Point out each malaria parasite.
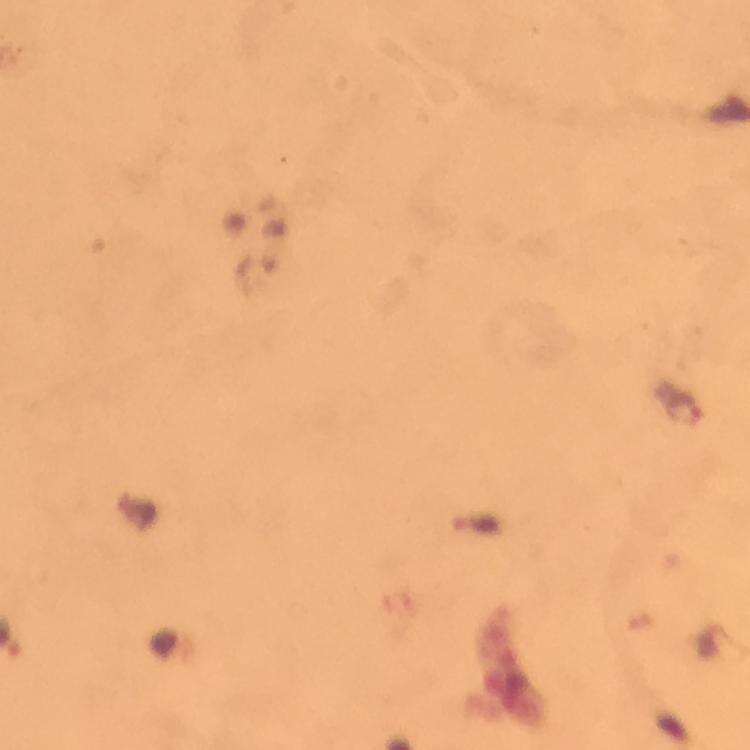

Approximate object centers, in pixels from the top-left corner.
Malaria parasites: (x=685, y=409).

At 100x magnification. Immersion oil applied. From a malaria diagnostic workup. A crop from one field of view. Giemsa-stained preparation. Image is 750×750 pixels. Thick smear. Photographed with a smartphone mounted on the microscope.